Give the extent of all Plasmodium ovale-infected red blood cells.
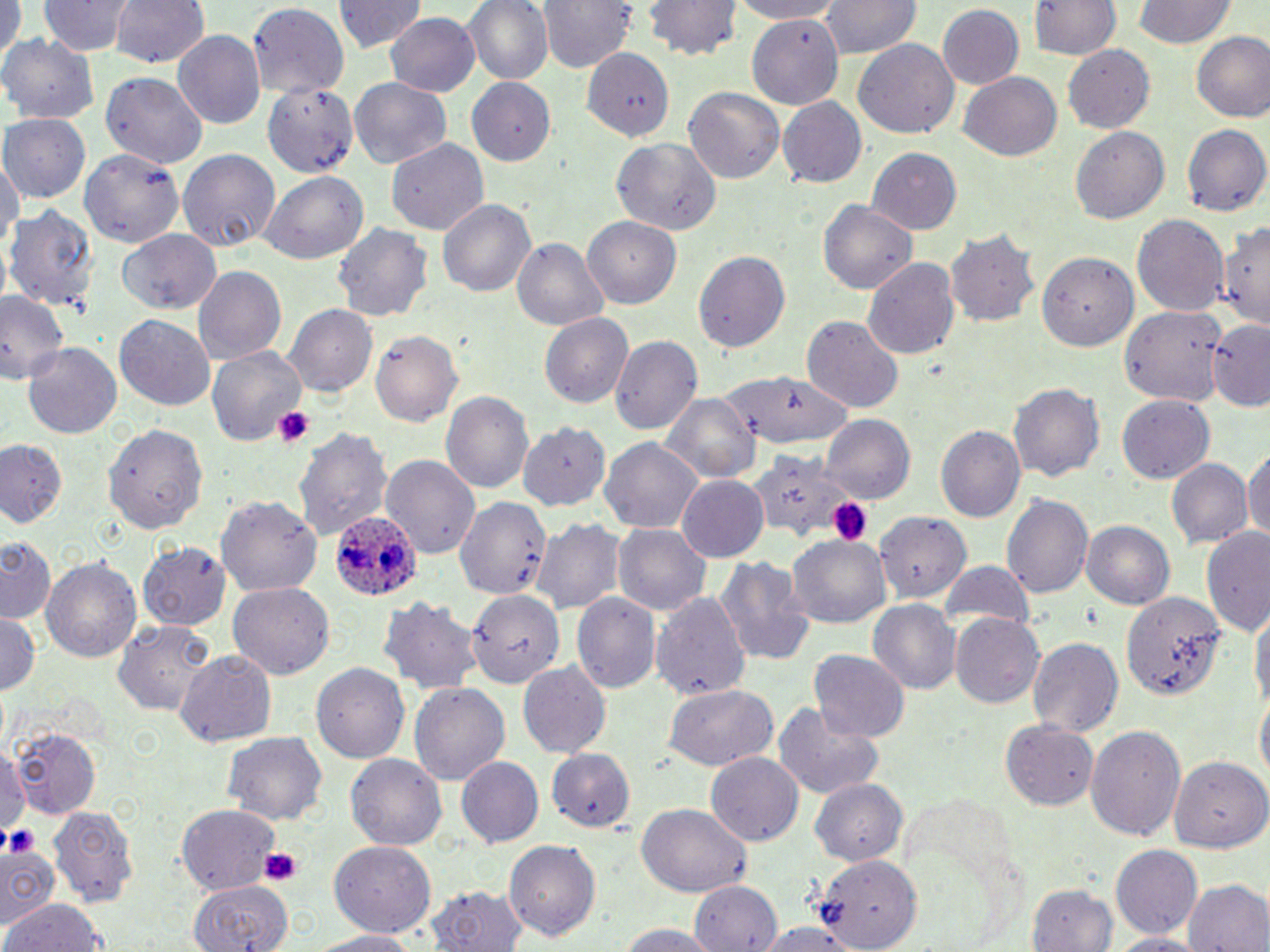
Approximate bounding boxes as named x1/y1/x2/y2 corners in pixels.
Plasmodium ovale-infected red blood cells: (x1=330, y1=509, x2=423, y2=601).

{
  "slide_level_diagnosis": "Plasmodium ovale",
  "magnification": "1000x",
  "uninfected_red_blood_cell_locations": "approximate bounding boxes as named x1/y1/x2/y2 corners in pixels: (x1=40, y1=0, x2=132, y2=57), (x1=107, y1=0, x2=211, y2=70), (x1=465, y1=0, x2=553, y2=85), (x1=541, y1=0, x2=638, y2=73), (x1=642, y1=0, x2=742, y2=59), (x1=724, y1=0, x2=849, y2=23), (x1=821, y1=0, x2=921, y2=60), (x1=1027, y1=0, x2=1123, y2=60), (x1=0, y1=1, x2=22, y2=70), (x1=334, y1=1, x2=422, y2=56), (x1=1133, y1=1, x2=1235, y2=49), (x1=246, y1=4, x2=350, y2=98), (x1=936, y1=5, x2=1025, y2=91), (x1=384, y1=12, x2=482, y2=96), (x1=746, y1=14, x2=847, y2=109), (x1=173, y1=29, x2=266, y2=126), (x1=1191, y1=31, x2=1270, y2=124), (x1=3, y1=35, x2=99, y2=123), (x1=853, y1=37, x2=961, y2=140), (x1=1062, y1=44, x2=1155, y2=132), (x1=580, y1=47, x2=673, y2=138), (x1=956, y1=71, x2=1061, y2=161), (x1=99, y1=74, x2=208, y2=168), (x1=261, y1=77, x2=358, y2=177), (x1=468, y1=77, x2=559, y2=165), (x1=349, y1=78, x2=452, y2=168), (x1=684, y1=86, x2=785, y2=187), (x1=776, y1=97, x2=868, y2=188), (x1=2, y1=115, x2=90, y2=203), (x1=1070, y1=122, x2=1169, y2=220), (x1=1182, y1=125, x2=1269, y2=216), (x1=385, y1=136, x2=487, y2=236), (x1=612, y1=137, x2=723, y2=238), (x1=79, y1=144, x2=184, y2=248), (x1=867, y1=145, x2=962, y2=232), (x1=177, y1=148, x2=280, y2=250), (x1=0, y1=149, x2=20, y2=259), (x1=258, y1=171, x2=368, y2=264), (x1=437, y1=196, x2=535, y2=297), (x1=819, y1=200, x2=914, y2=295), (x1=7, y1=203, x2=98, y2=314), (x1=1132, y1=213, x2=1230, y2=321), (x1=582, y1=217, x2=683, y2=308), (x1=1221, y1=219, x2=1270, y2=330), (x1=331, y1=222, x2=434, y2=323), (x1=946, y1=226, x2=1040, y2=328), (x1=118, y1=231, x2=218, y2=313), (x1=511, y1=238, x2=609, y2=331), (x1=1034, y1=248, x2=1140, y2=348), (x1=693, y1=250, x2=790, y2=352), (x1=864, y1=254, x2=960, y2=361), (x1=194, y1=265, x2=286, y2=364), (x1=0, y1=289, x2=67, y2=390), (x1=283, y1=304, x2=376, y2=397), (x1=1121, y1=304, x2=1229, y2=409), (x1=542, y1=313, x2=634, y2=408), (x1=114, y1=314, x2=215, y2=409), (x1=801, y1=314, x2=903, y2=412), (x1=1206, y1=318, x2=1270, y2=411), (x1=372, y1=329, x2=463, y2=427), (x1=611, y1=334, x2=702, y2=435), (x1=21, y1=342, x2=121, y2=442), (x1=207, y1=347, x2=303, y2=444), (x1=718, y1=372, x2=853, y2=451), (x1=1009, y1=381, x2=1104, y2=483), (x1=441, y1=390, x2=533, y2=497), (x1=659, y1=393, x2=759, y2=486), (x1=1116, y1=395, x2=1213, y2=484), (x1=821, y1=415, x2=914, y2=504), (x1=101, y1=421, x2=210, y2=535), (x1=521, y1=423, x2=609, y2=509), (x1=935, y1=424, x2=1025, y2=526), (x1=294, y1=426, x2=393, y2=544), (x1=601, y1=438, x2=702, y2=535), (x1=0, y1=442, x2=67, y2=528), (x1=1243, y1=447, x2=1270, y2=546), (x1=745, y1=449, x2=852, y2=544), (x1=381, y1=455, x2=481, y2=558), (x1=1168, y1=458, x2=1252, y2=549), (x1=675, y1=475, x2=770, y2=563), (x1=219, y1=494, x2=323, y2=597), (x1=1004, y1=494, x2=1096, y2=599), (x1=454, y1=495, x2=552, y2=605), (x1=871, y1=508, x2=971, y2=608), (x1=533, y1=519, x2=624, y2=615), (x1=1084, y1=520, x2=1175, y2=610), (x1=612, y1=521, x2=709, y2=614), (x1=1200, y1=530, x2=1270, y2=639), (x1=788, y1=535, x2=892, y2=630), (x1=139, y1=539, x2=231, y2=629), (x1=0, y1=540, x2=56, y2=626), (x1=719, y1=553, x2=816, y2=667), (x1=40, y1=555, x2=143, y2=665), (x1=937, y1=560, x2=1036, y2=633), (x1=227, y1=582, x2=334, y2=682), (x1=467, y1=588, x2=564, y2=691), (x1=652, y1=590, x2=752, y2=700), (x1=1120, y1=591, x2=1225, y2=701), (x1=573, y1=594, x2=659, y2=694), (x1=380, y1=597, x2=481, y2=695), (x1=868, y1=600, x2=960, y2=696), (x1=1251, y1=605, x2=1268, y2=720), (x1=0, y1=613, x2=42, y2=695), (x1=951, y1=613, x2=1044, y2=711), (x1=111, y1=618, x2=218, y2=713), (x1=1026, y1=635, x2=1124, y2=737), (x1=175, y1=649, x2=277, y2=748), (x1=809, y1=649, x2=911, y2=744), (x1=311, y1=662, x2=408, y2=765), (x1=516, y1=662, x2=611, y2=761), (x1=410, y1=682, x2=511, y2=787), (x1=660, y1=683, x2=780, y2=771), (x1=1255, y1=692, x2=1269, y2=789), (x1=772, y1=700, x2=888, y2=800), (x1=1002, y1=720, x2=1098, y2=809), (x1=12, y1=723, x2=102, y2=820), (x1=1085, y1=724, x2=1186, y2=842), (x1=223, y1=733, x2=328, y2=826), (x1=0, y1=741, x2=25, y2=841), (x1=547, y1=750, x2=636, y2=833), (x1=346, y1=753, x2=448, y2=853), (x1=707, y1=753, x2=803, y2=845), (x1=455, y1=756, x2=544, y2=849), (x1=1168, y1=757, x2=1266, y2=850), (x1=812, y1=779, x2=909, y2=865), (x1=47, y1=803, x2=139, y2=907), (x1=176, y1=803, x2=281, y2=893), (x1=635, y1=804, x2=751, y2=897), (x1=505, y1=840, x2=601, y2=943), (x1=327, y1=841, x2=438, y2=936), (x1=1110, y1=845, x2=1202, y2=937), (x1=1, y1=846, x2=61, y2=928), (x1=812, y1=854, x2=921, y2=948), (x1=690, y1=878, x2=782, y2=949), (x1=188, y1=880, x2=293, y2=952), (x1=1184, y1=880, x2=1270, y2=952), (x1=1028, y1=881, x2=1119, y2=951), (x1=427, y1=885, x2=529, y2=952), (x1=2, y1=897, x2=109, y2=952), (x1=612, y1=921, x2=725, y2=951), (x1=752, y1=922, x2=863, y2=950), (x1=312, y1=929, x2=420, y2=952), (x1=1107, y1=933, x2=1205, y2=952)",
  "image_size": "1270×952 pixels",
  "field_of_view": "single",
  "stain": "May-Grünwald-Giemsa",
  "platelet_locations": "approximate bounding boxes as named x1/y1/x2/y2 corners in pixels: (x1=273, y1=407, x2=313, y2=447), (x1=825, y1=495, x2=876, y2=545), (x1=4, y1=829, x2=37, y2=857), (x1=259, y1=846, x2=303, y2=884)",
  "modality": "optical microscopy",
  "preparation": "thin blood smear"
}